Locate every Plasmodium falciparum-infected red blood cell.
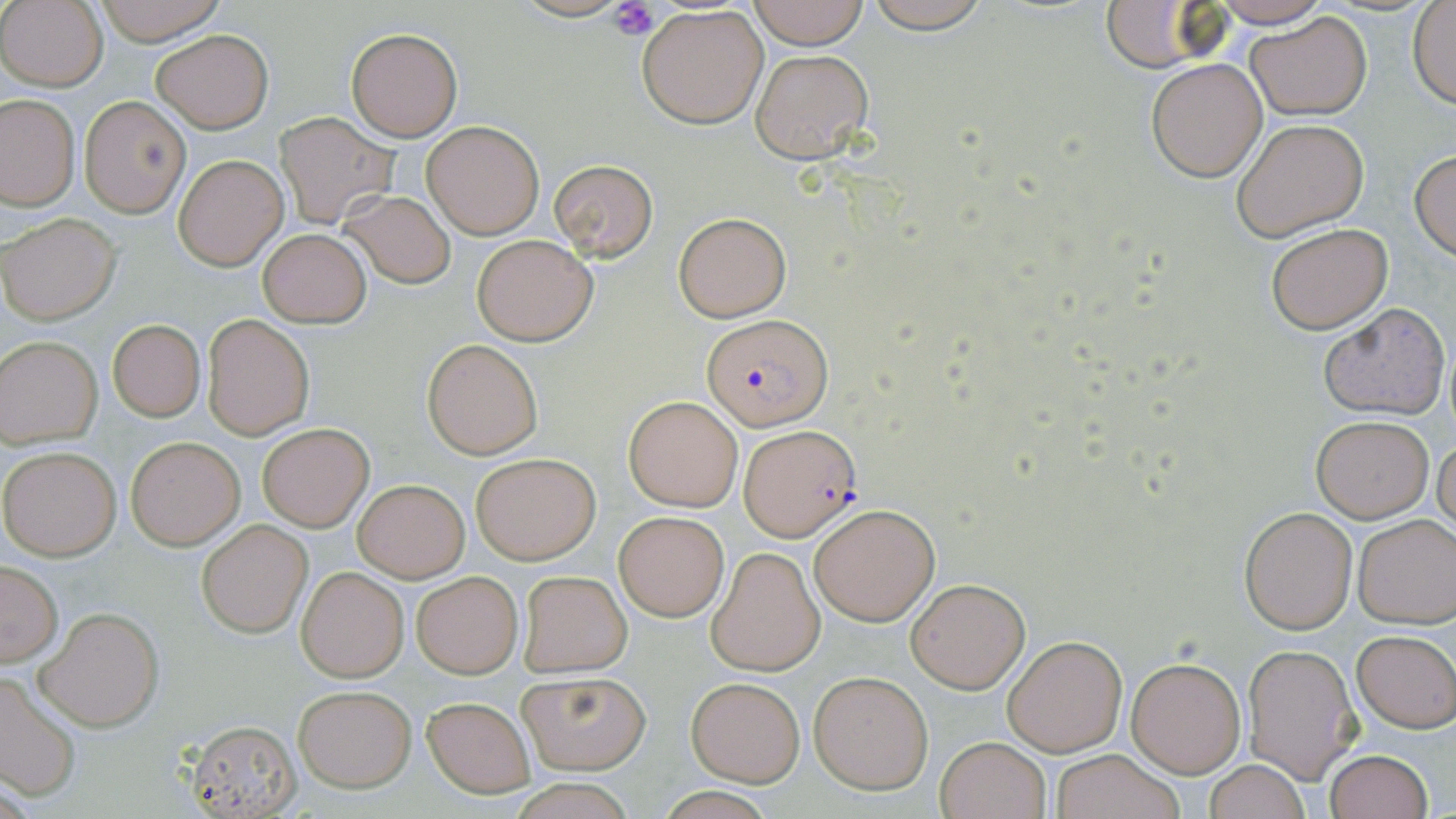
Approximate bounding boxes as (x1,y1)-(x2,y2) corner pairs in pixels.
Plasmodium falciparum-infected red blood cells: (704,313)-(830,431), (737,426)-(862,543).

Platelet locations: (608,0)-(659,42). Uninfected red blood cell locations: (91,0)-(229,45), (748,0)-(869,49), (862,0)-(995,32), (1209,0)-(1332,28), (1,1)-(107,89), (1407,2)-(1456,108), (1094,3)-(1221,74), (638,5)-(769,129), (1245,12)-(1371,121), (347,27)-(462,141), (151,29)-(273,131), (749,48)-(873,162), (1146,57)-(1268,182), (1,93)-(79,211), (79,95)-(190,217), (272,111)-(399,229), (1231,117)-(1370,241), (420,119)-(544,238), (1410,148)-(1456,260), (174,154)-(286,270), (550,158)-(657,260), (337,190)-(457,290), (674,211)-(791,322), (1,213)-(120,324), (1266,222)-(1393,334), (258,228)-(372,327), (473,234)-(597,346), (1319,302)-(1449,421), (202,314)-(314,440), (107,320)-(205,422), (0,335)-(102,446), (422,338)-(542,459), (623,396)-(743,512), (1310,414)-(1434,522), (258,423)-(374,531), (1434,430)-(1456,541), (126,437)-(244,549), (0,446)-(120,560), (470,453)-(600,564), (353,479)-(469,582), (809,501)-(941,626), (1240,508)-(1357,633), (613,509)-(729,622), (1352,513)-(1456,628), (197,520)-(312,639), (707,547)-(825,676), (1,561)-(63,666), (297,567)-(409,682), (517,570)-(633,677), (411,571)-(524,679), (905,577)-(1030,693), (34,605)-(165,732), (1352,629)-(1456,733), (1002,635)-(1126,756), (1241,644)-(1362,781), (1127,657)-(1245,778), (516,670)-(650,775), (0,672)-(81,802), (809,672)-(932,793), (686,676)-(805,786), (292,685)-(417,792), (420,694)-(537,799), (184,720)-(303,816), (935,735)-(1051,819), (1323,749)-(1434,819), (1050,750)-(1184,819), (1203,759)-(1310,819). Slide-level diagnosis: Plasmodium falciparum. Light microscopy. Thin blood smear. 1000x magnification. Image is 1456×819 pixels. One field of a larger specimen. May-Grünwald-Giemsa stain.